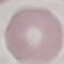 Malaria status: uninfected. Acquired by smartphone through the microscope eyepiece. Thin blood smear. Cell patch, automatically extracted from a larger field of view and resized to 64 × 64 pixels. Giemsa-stained preparation.